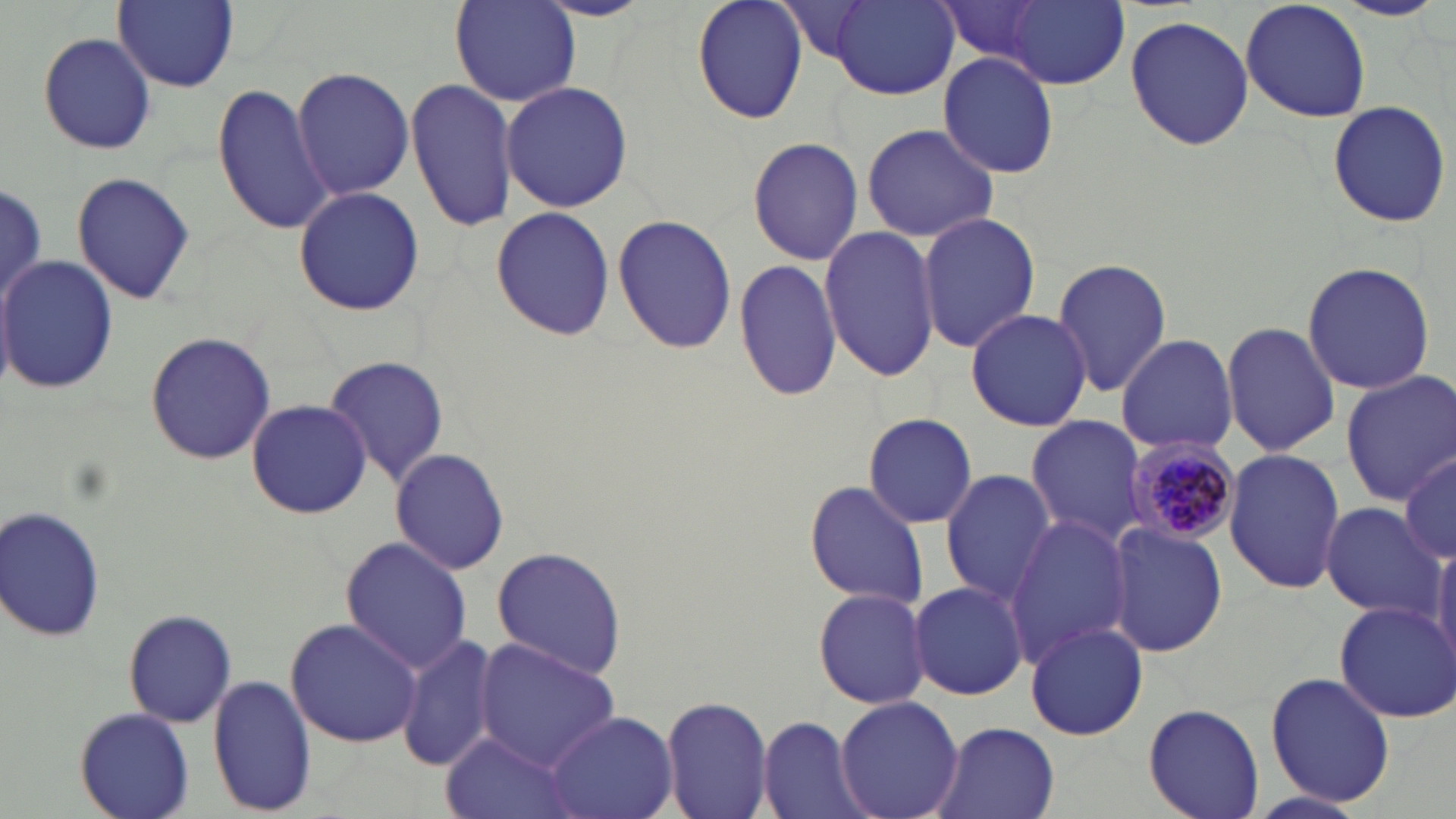

Summary:
  - Coordinate format: approximate bounding boxes as named x1/y1/x2/y2 corners in pixels
  - Plasmodium malariae-infected red blood cell locations: (x1=1127, y1=437, x2=1241, y2=545)
  - Uninfected red blood cell locations: (x1=113, y1=0, x2=239, y2=90), (x1=694, y1=0, x2=809, y2=123), (x1=1242, y1=0, x2=1371, y2=123), (x1=449, y1=1, x2=581, y2=108), (x1=997, y1=1, x2=1129, y2=88), (x1=828, y1=2, x2=958, y2=99), (x1=935, y1=2, x2=1060, y2=69), (x1=1125, y1=15, x2=1254, y2=150), (x1=38, y1=33, x2=155, y2=154), (x1=937, y1=52, x2=1061, y2=178), (x1=292, y1=65, x2=412, y2=201), (x1=407, y1=79, x2=518, y2=233), (x1=500, y1=81, x2=633, y2=213), (x1=211, y1=84, x2=337, y2=237), (x1=1325, y1=99, x2=1452, y2=229), (x1=861, y1=125, x2=999, y2=242), (x1=747, y1=135, x2=866, y2=266), (x1=72, y1=171, x2=195, y2=306), (x1=3, y1=178, x2=46, y2=312), (x1=293, y1=185, x2=424, y2=317), (x1=490, y1=207, x2=616, y2=340), (x1=916, y1=210, x2=1041, y2=354), (x1=613, y1=213, x2=737, y2=355), (x1=819, y1=225, x2=942, y2=382), (x1=0, y1=255, x2=118, y2=398), (x1=1052, y1=257, x2=1173, y2=400), (x1=733, y1=259, x2=843, y2=400), (x1=1301, y1=260, x2=1436, y2=395), (x1=965, y1=307, x2=1093, y2=430), (x1=1220, y1=319, x2=1342, y2=456), (x1=145, y1=331, x2=278, y2=467), (x1=1116, y1=333, x2=1239, y2=455), (x1=321, y1=353, x2=448, y2=486), (x1=1340, y1=370, x2=1456, y2=505), (x1=245, y1=397, x2=372, y2=520), (x1=860, y1=413, x2=980, y2=530), (x1=1024, y1=416, x2=1144, y2=544), (x1=389, y1=448, x2=511, y2=575), (x1=1223, y1=448, x2=1346, y2=595), (x1=1400, y1=452, x2=1456, y2=565), (x1=940, y1=469, x2=1058, y2=606), (x1=804, y1=480, x2=930, y2=611), (x1=0, y1=503, x2=107, y2=645), (x1=1319, y1=503, x2=1448, y2=620), (x1=1005, y1=514, x2=1137, y2=666), (x1=1104, y1=521, x2=1230, y2=657), (x1=339, y1=536, x2=476, y2=674), (x1=1430, y1=542, x2=1456, y2=668), (x1=488, y1=546, x2=628, y2=678), (x1=909, y1=580, x2=1030, y2=701), (x1=814, y1=586, x2=929, y2=711), (x1=1334, y1=601, x2=1456, y2=721), (x1=123, y1=607, x2=238, y2=729), (x1=287, y1=616, x2=419, y2=749), (x1=1025, y1=620, x2=1148, y2=742), (x1=399, y1=632, x2=500, y2=773), (x1=475, y1=639, x2=622, y2=774), (x1=1266, y1=671, x2=1394, y2=806), (x1=207, y1=677, x2=317, y2=814), (x1=660, y1=694, x2=775, y2=819), (x1=835, y1=694, x2=963, y2=819), (x1=1144, y1=703, x2=1264, y2=819), (x1=75, y1=706, x2=194, y2=818), (x1=543, y1=711, x2=677, y2=819), (x1=757, y1=716, x2=870, y2=819), (x1=930, y1=723, x2=1062, y2=819), (x1=440, y1=732, x2=585, y2=819)
  - Slide-level diagnosis: Plasmodium malariae
  - Magnification: 1000x
  - Preparation: thin blood smear
  - Image size: 1456×819 pixels
  - Modality: optical microscopy
  - Field of view: one of a larger specimen
  - Stain: May-Grünwald-Giemsa